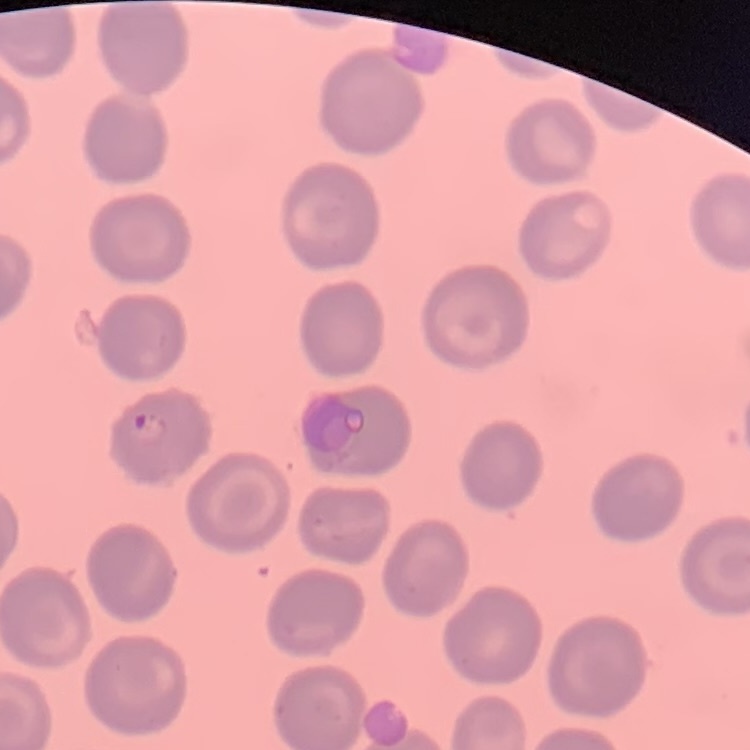

The red blood cells show no rouleaux formation. Thin blood smear. Field's or Giemsa stain. One tile cut from a larger photomicrograph.